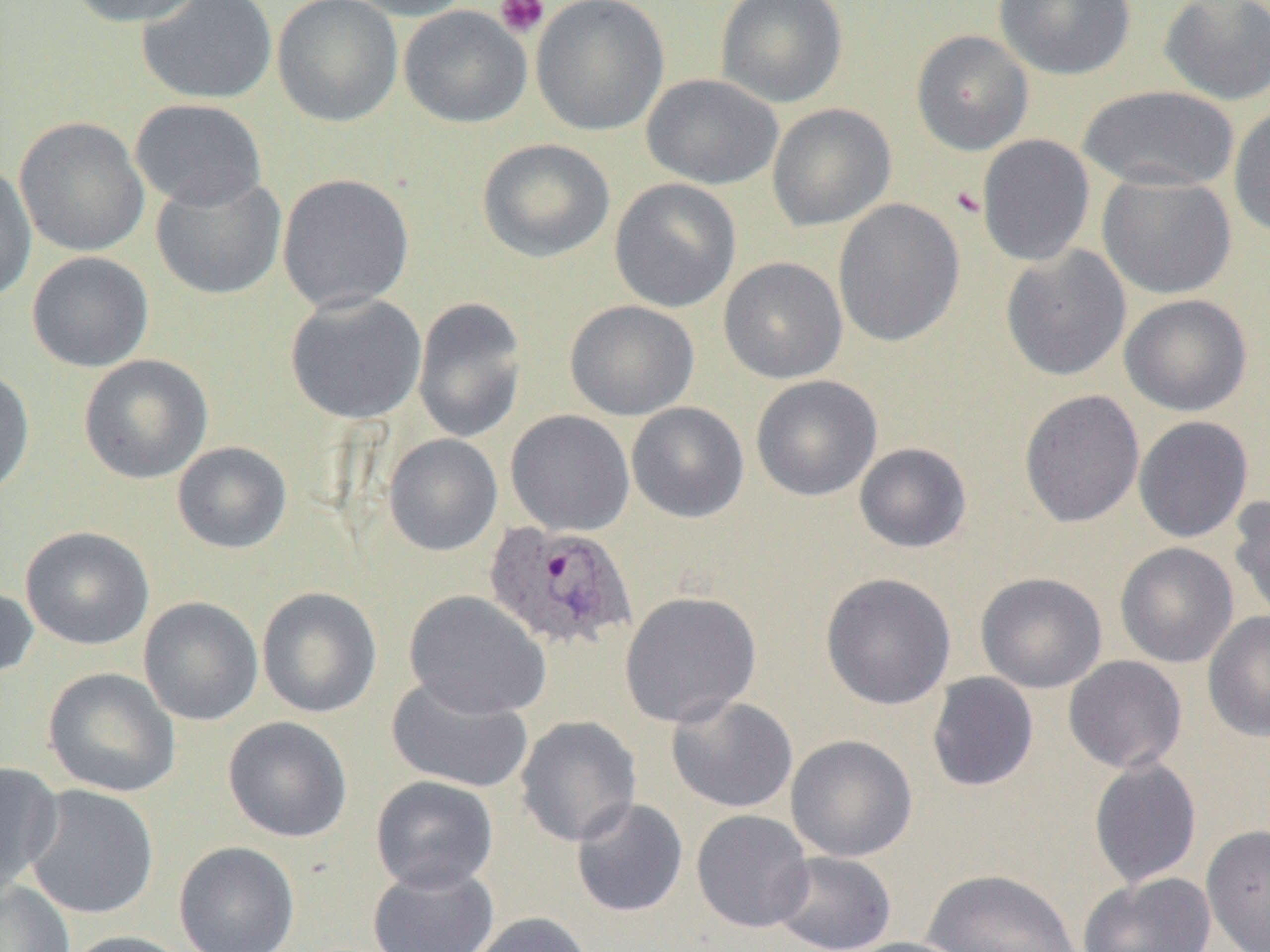
Summary:
  - Coordinate format: approximate bounding boxes as (x1,y1)-(x2,y2) corner pairs in pixels
  - Plasmodium ovale-infected red blood cell locations: (482,521)-(638,653)
  - Uninfected red blood cell locations: (68,0)-(205,27), (136,0)-(278,105), (271,0)-(403,128), (341,0)-(476,21), (531,0)-(669,136), (715,0)-(849,108), (994,0)-(1137,80), (1158,0)-(1270,105), (398,5)-(532,128), (911,29)-(1033,155), (641,73)-(783,189), (1078,85)-(1239,193), (129,98)-(267,211), (766,103)-(897,232), (1228,104)-(1270,239), (13,116)-(150,256), (976,134)-(1095,267), (477,138)-(615,263), (0,162)-(37,302), (1097,172)-(1237,299), (150,173)-(286,300), (277,173)-(415,313), (609,178)-(741,313), (832,198)-(965,348), (1000,245)-(1132,381), (26,251)-(154,372), (718,257)-(848,383), (284,292)-(427,425), (1119,293)-(1252,416), (412,296)-(528,443), (564,300)-(699,421), (78,354)-(214,484), (0,365)-(34,501), (750,375)-(882,501), (1018,389)-(1145,528), (626,401)-(749,523), (505,410)-(635,536), (1133,416)-(1254,543), (382,433)-(503,556), (171,441)-(292,554), (853,442)-(972,553), (1228,493)-(1270,624), (20,526)-(154,650), (1115,542)-(1239,668), (821,572)-(956,710), (976,572)-(1107,693), (0,584)-(38,682), (256,586)-(382,718), (403,590)-(551,719), (619,590)-(762,728), (138,597)-(264,726), (1203,610)-(1270,742), (1063,655)-(1187,774), (42,667)-(181,798), (926,672)-(1039,792), (386,675)-(534,793), (666,695)-(799,813), (222,715)-(352,843), (514,716)-(642,846), (785,734)-(918,862), (1089,758)-(1202,888), (1,762)-(62,894), (370,776)-(499,893), (23,785)-(160,920), (570,798)-(689,918), (691,809)-(814,933), (1201,823)-(1270,952), (174,840)-(300,952), (770,850)-(897,952), (367,864)-(499,952), (922,868)-(1082,951), (1078,871)-(1216,952), (0,880)-(75,952), (467,911)-(595,952), (59,930)-(194,952), (841,937)-(975,952)
  - Platelet locations: (494,0)-(550,39)
  - Slide-level diagnosis: Plasmodium ovale
  - Field of view: single
  - Modality: optical microscopy
  - Image size: 1270×952 pixels
  - Preparation: thin blood smear
  - Magnification: 1000x